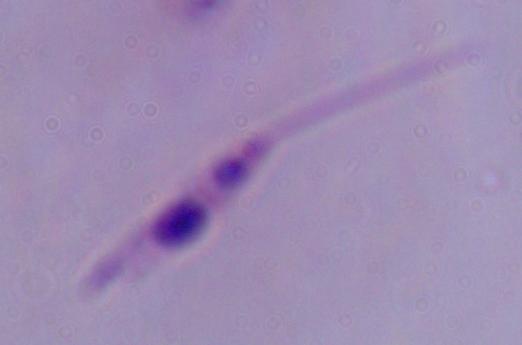
identification = Leishmania
magnification = 1000x
modality = photomicrograph